State which parasite is depicted.
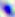
Toxoplasma gondii.

Summary:
  - Modality: photomicrograph
  - Magnification: 400x